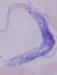
modality = photomicrograph
magnification = 1000x
identification = trypanosome